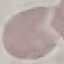

Result: negative for malaria parasites. Thin blood smear. Giemsa stain. Automatically extracted cell patch, resized to 64 × 64 pixels. Photographed with a smartphone camera at the microscope eyepiece.